State which parasite is depicted.
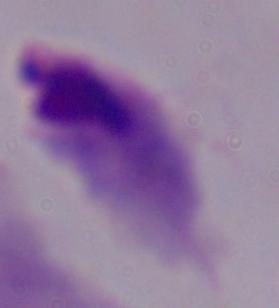
This is a trichomonad.

Summary:
  - Modality: photomicrograph
  - Magnification: 1000x